Name the blood parasite species.
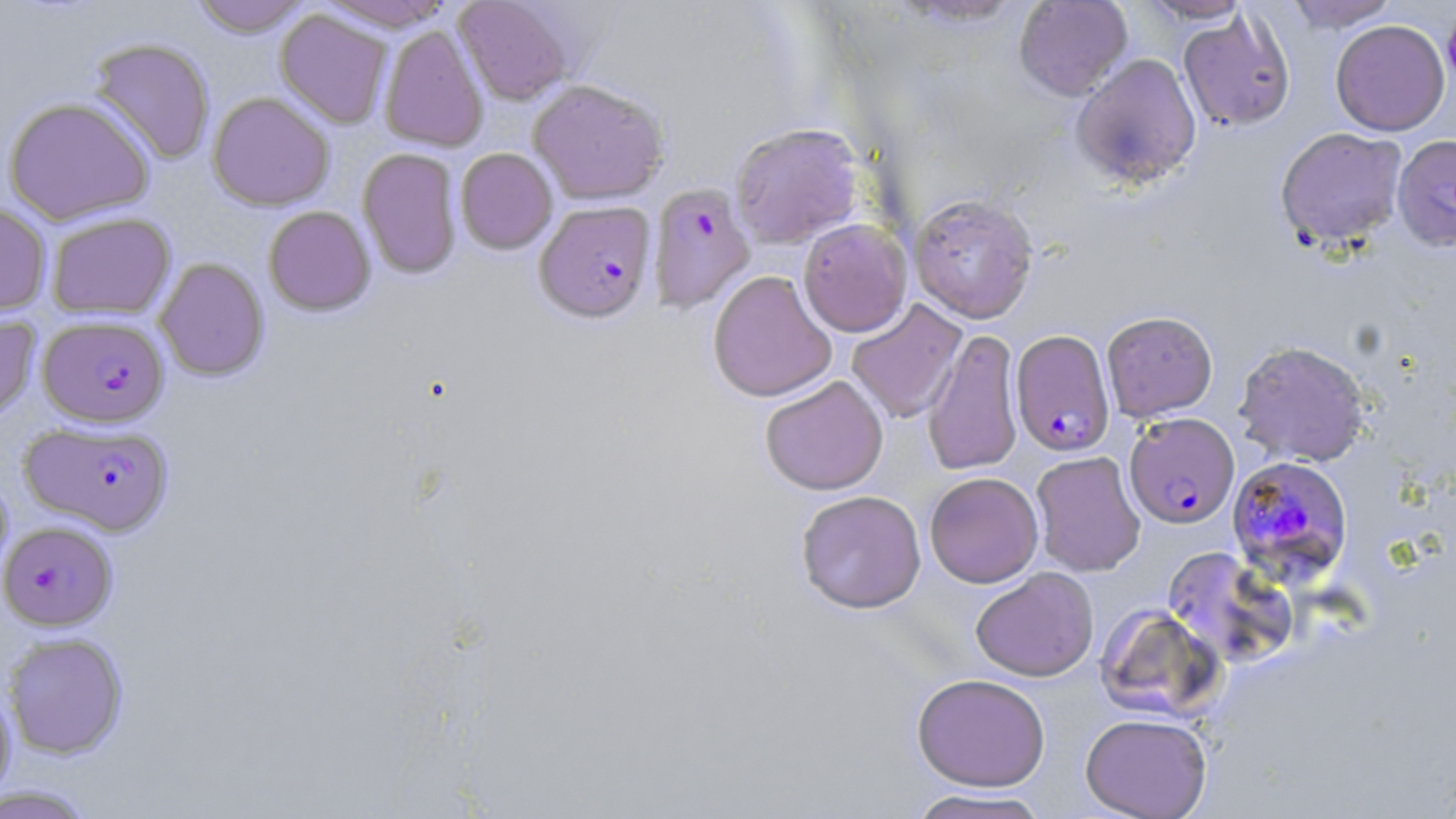
Plasmodium falciparum.

preparation = thin blood smear
Plasmodium falciparum-infected red blood cell locations = approximate bounding boxes as [x1, y1, x2, y2] in pixels: [648, 182, 755, 313], [534, 201, 656, 323], [38, 315, 169, 428], [1010, 329, 1116, 457], [1124, 412, 1240, 530], [19, 420, 174, 536], [1225, 455, 1354, 588], [1, 522, 117, 632]
magnification = 1000x
uninfected red blood cell locations = approximate bounding boxes as [x1, y1, x2, y2] in pixels: [189, 0, 311, 38], [314, 0, 456, 32], [454, 0, 574, 105], [1013, 0, 1133, 100], [1138, 0, 1253, 23], [1284, 0, 1401, 32], [275, 9, 393, 128], [1178, 10, 1296, 132], [1331, 19, 1450, 136], [379, 24, 488, 152], [87, 37, 216, 165], [1072, 53, 1201, 190], [527, 79, 669, 206], [207, 92, 334, 211], [3, 97, 154, 226], [730, 123, 863, 249], [1275, 126, 1409, 249], [1392, 134, 1456, 252], [358, 148, 462, 279], [455, 148, 557, 254], [909, 193, 1039, 324], [0, 202, 51, 317], [264, 206, 375, 316], [46, 213, 176, 320], [797, 219, 913, 337], [154, 258, 269, 381], [708, 270, 836, 403], [846, 299, 968, 424], [1101, 310, 1218, 421], [0, 315, 40, 422], [922, 329, 1023, 476], [1233, 339, 1371, 467], [760, 375, 889, 495], [1030, 451, 1146, 577], [924, 472, 1043, 587], [795, 490, 927, 613], [1162, 547, 1297, 668], [970, 567, 1099, 681], [1095, 603, 1224, 723], [3, 633, 128, 760], [911, 673, 1050, 791], [0, 682, 16, 805], [1080, 712, 1212, 819], [0, 784, 97, 819], [907, 788, 1051, 818]
field of view = one of a larger specimen
image size = 1456×819 pixels
stain = May-Grünwald-Giemsa
modality = optical microscopy